Outline each P. falciparum parasite and classify it by life-cycle stage.
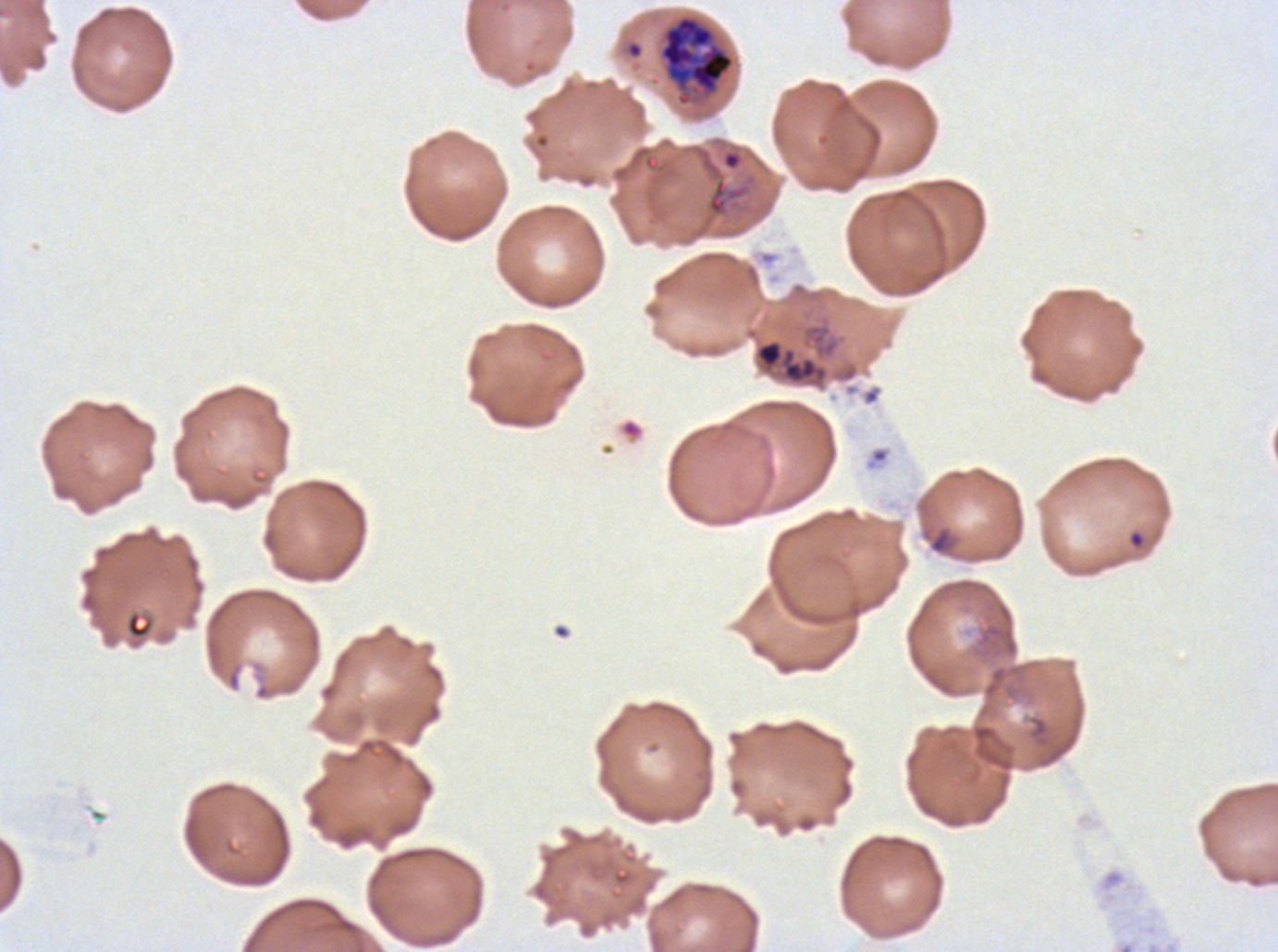
Approximate bounding boxes as {x1, y1, x2, y2} in pixels.
Rings: {1127, 530, 1146, 550}.
Early schizonts: {659, 15, 734, 95}.
No late-ring/early-trophozoite forms, mid trophozoites, late trophozoites, late schizonts, segmenters, or gametocytes observed.

{
  "preparation": "thin blood film",
  "life_cycle_stages_observed": "ring, early schizont",
  "stain": "Giemsa",
  "image_size": "1278×952 pixels",
  "specimen": "P. falciparum from a patient in The Gambia, cultured ex vivo for 24 to 48 hours",
  "field_of_view": "sub-image separated from a larger composite",
  "debris_locations": "approximate bounding boxes as {x1, y1, x2, y2} in pixels: {755, 339, 827, 384}, {928, 526, 955, 555}"
}